Assess this cell for malaria.
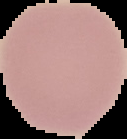
Uninfected.

image size = 127×139 pixels
preparation = thin blood smear
image type = segmented cell region with the area outside set to black